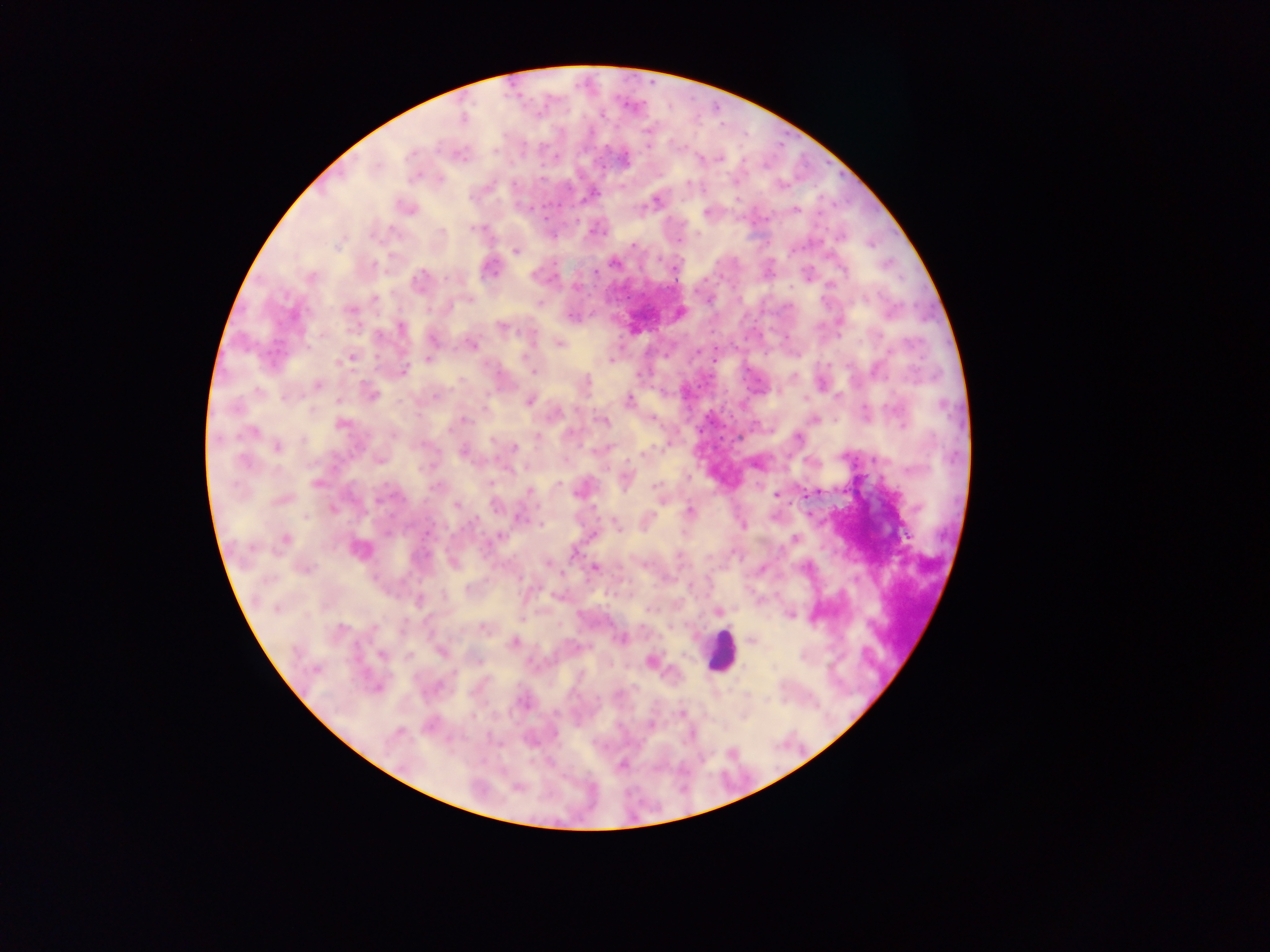

Approximate centers as x y in pixels.
Summary:
  - Malaria parasite locations: 462 119; 647 130; 459 153; 623 158; 720 158; 591 194; 655 200; 406 207; 795 210; 707 213; 475 228; 600 231; 679 241; 634 246; 515 251; 614 263; 489 268; 675 269; 310 277; 419 283; 349 309; 679 312; 839 321; 400 327; 502 327; 432 338; 558 343; 471 345; 350 357; 428 359; 612 360; 534 371; 402 372; 586 383; 317 385; 780 391; 370 394; 435 395; 805 398; 528 399; 628 400; 463 419; 814 419; 604 421; 340 424; 251 432; 797 437; 537 438; 492 439; 277 447; 514 448; 464 451; 625 480; 317 483; 435 486; 656 486; 528 490; 810 493; 775 495; 281 499; 662 501; 495 505; 457 506; 333 509; 690 512; 519 518; 616 523; 542 524; 742 526; 428 534; 498 536; 795 538; 284 539; 359 549; 574 553; 452 562; 549 563; 644 564; 303 567; 594 567; 419 601; 718 611; 789 614; 484 627; 621 638; 751 640; 513 642; 441 651; 381 654; 477 660; 651 661; 316 669; 377 687; 618 693; 679 713; 650 725; 621 765; 516 787
  - Leukocyte locations: 720 652
  - Field of view: single
  - Preparation: thick blood smear
  - Country: Ghana
  - Image size: 1270×952 pixels
  - Capture: mobile-phone photograph through a microscope